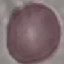 Malaria status: uninfected. Cell patch, automatically extracted from a larger field of view and resized to 64 × 64 pixels. Acquired by smartphone through the microscope eyepiece. Thin blood film. Giemsa stain.